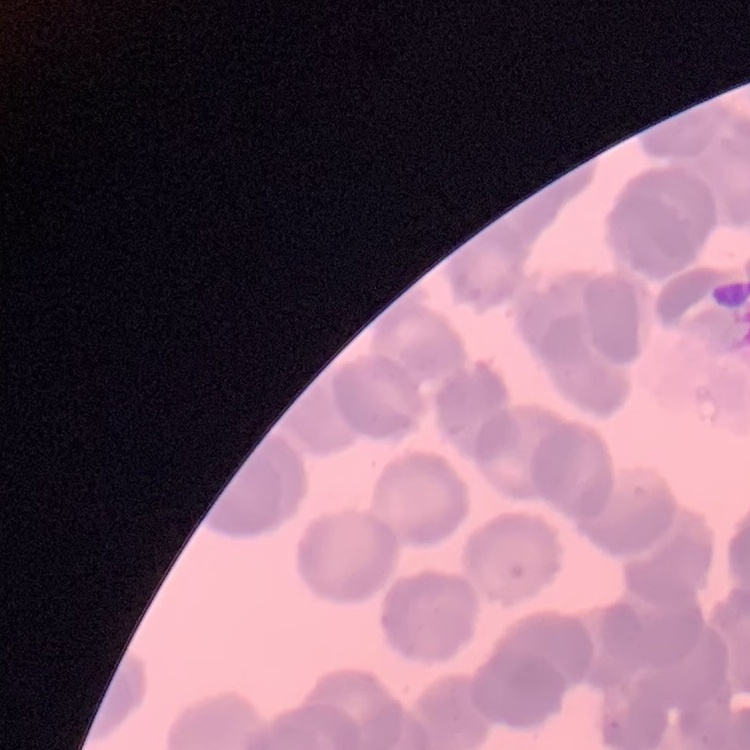
The erythrocytes show rouleaux formation. Field's or Giemsa stain. Square crop of a larger photomicrograph. Thin blood smear.